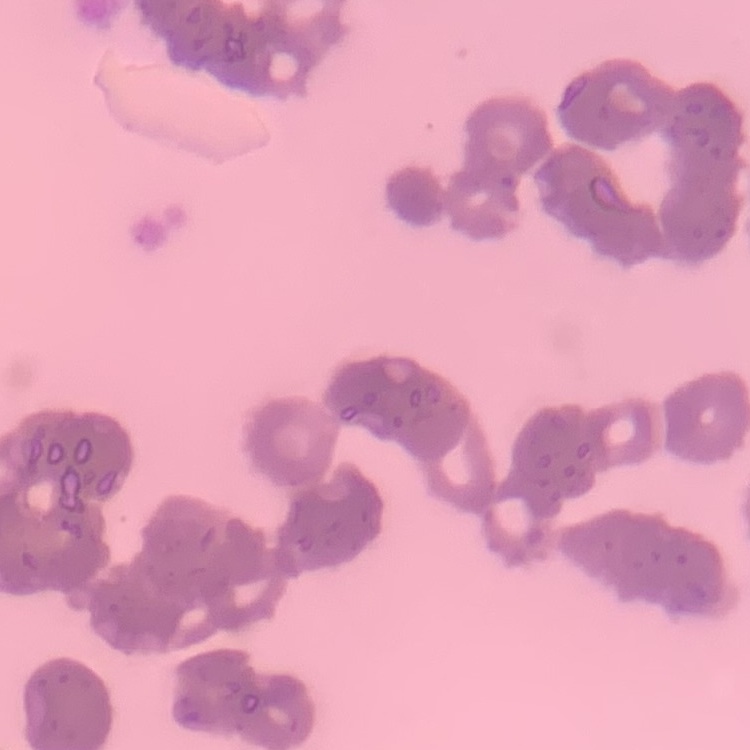
The erythrocytes show rouleaux formation. Stained with either Field's or Giemsa. Thin blood film. Square crop of a larger photomicrograph.